Name the cell type shown.
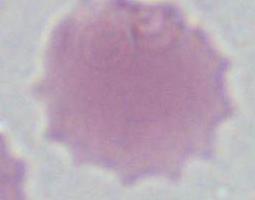

An erythrocyte.

{
  "modality": "micrograph",
  "magnification": "1000x"
}